Classify this cell by malaria status.
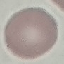
It is uninfected.

Thin smear of blood. Cell patch, automatically extracted from a larger field of view and resized to 64 × 64 pixels. Acquired by smartphone through the microscope eyepiece. Giemsa stain.